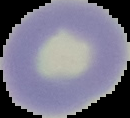
Summary:
  - Preparation: thin blood film
  - Result: no Plasmodium parasites seen
  - Image type: segmented cell region on a black background
  - Image size: 130×118 pixels